Give the extent of all uninfected red blood cells.
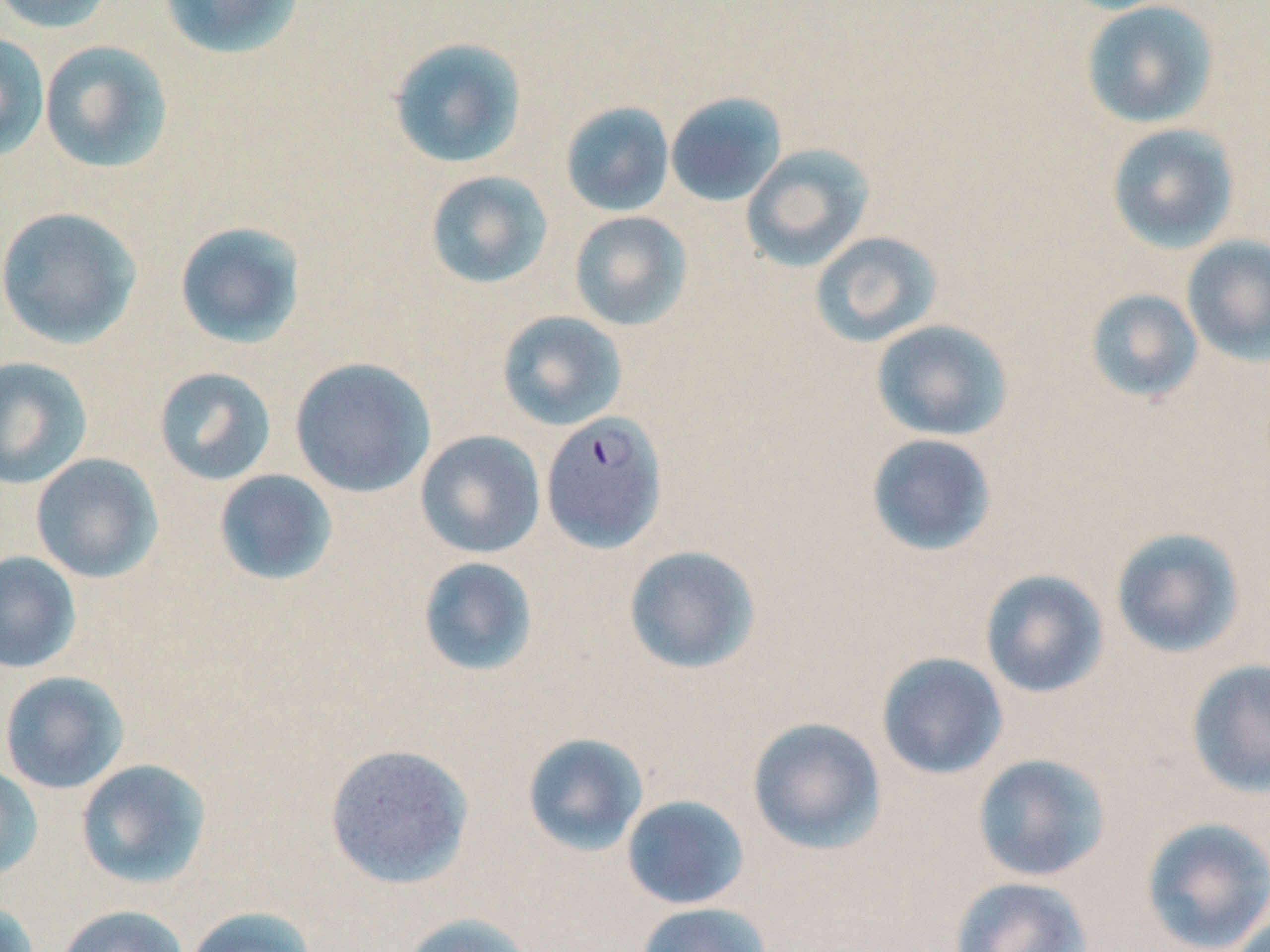
Approximate bounding boxes as (x1,y1)-(x2,y2) corner pairs in pixels.
Uninfected red blood cells: (0,0)-(117,35), (158,0)-(306,61), (1080,0)-(1220,129), (0,32)-(50,161), (387,36)-(528,169), (39,39)-(174,174), (665,91)-(787,207), (560,101)-(675,217), (1106,123)-(1239,254), (741,143)-(875,271), (424,170)-(554,290), (0,206)-(142,349), (568,210)-(693,331), (174,221)-(307,349), (810,230)-(944,348), (1181,235)-(1270,365), (1085,289)-(1203,403), (496,310)-(628,431), (871,319)-(1013,442), (0,356)-(93,489), (289,357)-(435,498), (153,367)-(277,486), (415,430)-(546,559), (865,433)-(998,557), (30,453)-(163,583), (212,469)-(339,587), (1110,526)-(1247,659), (623,544)-(762,675), (0,551)-(81,674), (416,556)-(539,677), (979,568)-(1109,698), (876,652)-(1008,780), (1186,658)-(1270,798), (1,671)-(131,794), (747,717)-(887,855), (521,732)-(649,857), (324,743)-(475,890), (971,753)-(1112,883), (75,758)-(212,889), (0,764)-(43,881), (620,794)-(750,910), (1139,815)-(1270,952), (948,876)-(1093,952), (0,899)-(39,952), (635,901)-(772,952), (56,904)-(189,952), (183,905)-(318,952), (398,912)-(536,952).

Plasmodium falciparum-infected red blood cell locations: (540,410)-(668,554). Slide-level diagnosis: Plasmodium falciparum. Thin blood smear. Image is 1270×952 pixels. Light microscopy. May-Grünwald-Giemsa-stained preparation. 1000x magnification. Single field of view.